Name the parasite shown.
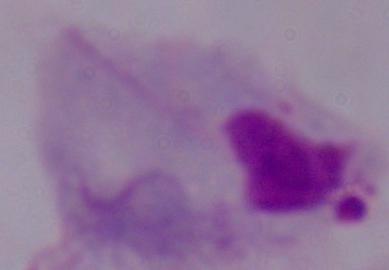

A trichomonad.

Photomicrograph. Captured at 1000x magnification.